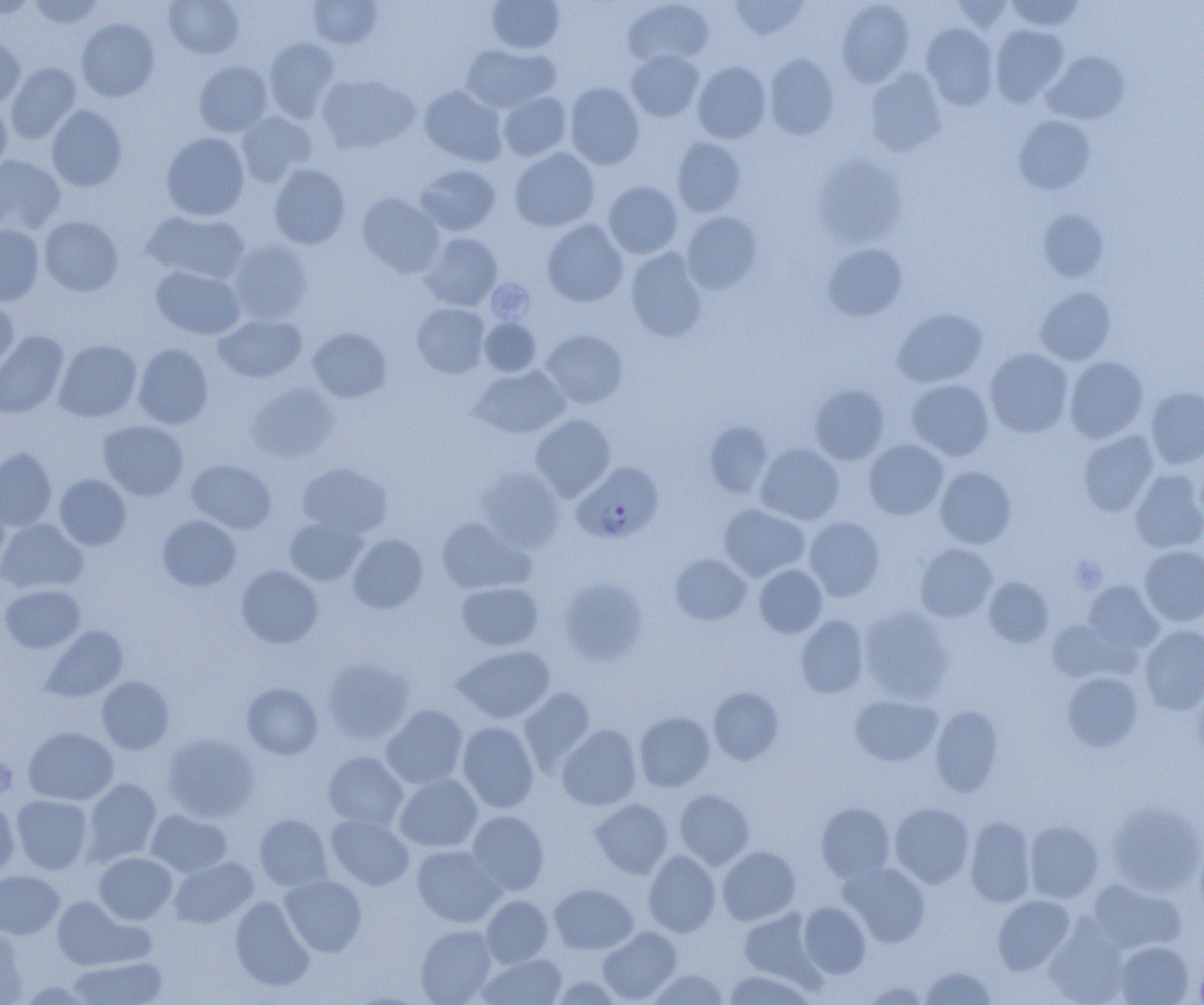

Approximate bounding boxes as (x1, y1, x2, y2) in pixels. Platelet locations: (487, 279, 534, 322), (1069, 557, 1106, 593), (0, 756, 16, 798). Plasmodium falciparum-infected red blood cell locations: (573, 462, 663, 542). Uninfected red blood cell locations: (0, 0, 39, 19), (27, 0, 103, 29), (163, 0, 244, 59), (306, 0, 383, 48), (486, 0, 565, 54), (623, 0, 714, 69), (729, 0, 809, 40), (1006, 0, 1084, 31), (837, 1, 915, 87), (951, 1, 1016, 33), (76, 18, 159, 101), (921, 23, 998, 110), (989, 24, 1069, 107), (0, 37, 25, 107), (263, 37, 339, 121), (460, 44, 558, 112), (626, 50, 705, 122), (1042, 51, 1130, 124), (765, 54, 840, 140), (194, 60, 273, 137), (692, 61, 771, 143), (5, 62, 81, 144), (865, 68, 946, 157), (316, 74, 419, 154), (565, 82, 645, 169), (419, 85, 507, 166), (498, 91, 571, 161), (0, 101, 12, 171), (47, 105, 127, 190), (235, 111, 317, 186), (1014, 115, 1096, 195), (161, 132, 250, 220), (672, 136, 746, 217), (509, 147, 600, 231), (0, 154, 66, 234), (814, 155, 908, 247), (269, 164, 351, 249), (415, 164, 501, 236), (603, 181, 683, 259), (356, 193, 444, 277), (1039, 209, 1109, 282), (143, 210, 249, 284), (680, 211, 762, 294), (39, 215, 123, 296), (541, 219, 628, 307), (0, 224, 44, 305), (420, 233, 502, 311), (229, 239, 312, 323), (822, 243, 908, 321), (625, 248, 708, 342), (151, 265, 245, 339), (1035, 287, 1117, 365), (0, 297, 19, 375), (412, 303, 490, 378), (892, 307, 987, 388), (213, 313, 307, 383), (479, 318, 541, 376), (307, 327, 391, 402), (540, 329, 628, 409), (0, 330, 68, 418), (54, 339, 142, 422), (133, 344, 213, 428), (984, 347, 1074, 437), (1064, 356, 1148, 442), (470, 365, 569, 439), (906, 379, 994, 461), (247, 382, 339, 463), (809, 383, 890, 464), (1145, 387, 1204, 468), (531, 414, 615, 501), (98, 420, 188, 500), (704, 421, 774, 498), (1078, 430, 1158, 516), (864, 439, 948, 520), (755, 443, 844, 525), (0, 448, 57, 531), (186, 459, 276, 534), (297, 462, 392, 537), (477, 466, 564, 552), (935, 466, 1016, 548), (1130, 469, 1204, 553), (54, 474, 131, 550), (719, 504, 810, 581), (157, 515, 241, 591), (284, 516, 368, 586), (804, 516, 884, 601), (436, 517, 533, 594), (0, 518, 88, 593), (348, 534, 427, 613), (915, 543, 997, 622), (1140, 545, 1204, 626), (670, 553, 751, 625), (754, 564, 827, 638), (236, 565, 323, 648), (556, 577, 647, 665), (983, 577, 1054, 647), (1082, 581, 1163, 655), (456, 582, 544, 651), (1, 584, 85, 653), (858, 605, 954, 703), (796, 615, 868, 698), (1048, 618, 1134, 683), (41, 625, 128, 702), (1139, 625, 1204, 714), (454, 645, 555, 723), (321, 657, 414, 744), (1062, 671, 1143, 751), (96, 677, 174, 753), (242, 682, 323, 759), (708, 687, 784, 765), (519, 688, 596, 770), (850, 694, 942, 766), (381, 705, 469, 789), (930, 705, 1004, 797), (634, 711, 714, 791), (457, 722, 539, 813), (557, 724, 642, 811), (23, 727, 118, 805), (162, 733, 259, 822), (323, 751, 408, 831), (394, 773, 483, 852), (82, 778, 161, 864), (674, 788, 754, 869), (11, 795, 93, 874), (590, 798, 673, 879), (0, 799, 19, 879), (1105, 801, 1204, 896), (815, 802, 895, 882), (889, 802, 974, 887), (146, 810, 232, 877), (467, 810, 548, 896), (254, 814, 333, 891), (326, 814, 414, 891), (965, 816, 1036, 906), (1024, 821, 1103, 903), (412, 845, 504, 927), (717, 846, 800, 924), (643, 849, 721, 936), (94, 852, 177, 924), (169, 857, 258, 928), (840, 861, 931, 946), (0, 871, 64, 939), (280, 875, 367, 957), (1086, 879, 1186, 953), (549, 883, 637, 954), (992, 894, 1075, 973), (229, 895, 314, 991), (481, 895, 553, 967), (51, 896, 147, 970), (798, 902, 871, 978), (739, 909, 818, 985), (1045, 921, 1130, 1005), (415, 925, 496, 1004), (0, 926, 27, 1005), (598, 926, 681, 1004), (1114, 941, 1194, 1005), (478, 953, 567, 1005), (68, 955, 167, 1004), (920, 966, 997, 1005), (648, 969, 728, 1004), (722, 969, 816, 1004), (551, 975, 625, 1005), (860, 981, 930, 1004). Slide-level diagnosis: Plasmodium falciparum. Optical microscopy. Thin blood film. Image is 1204×1005 pixels. 1000x magnification. Single field of view.